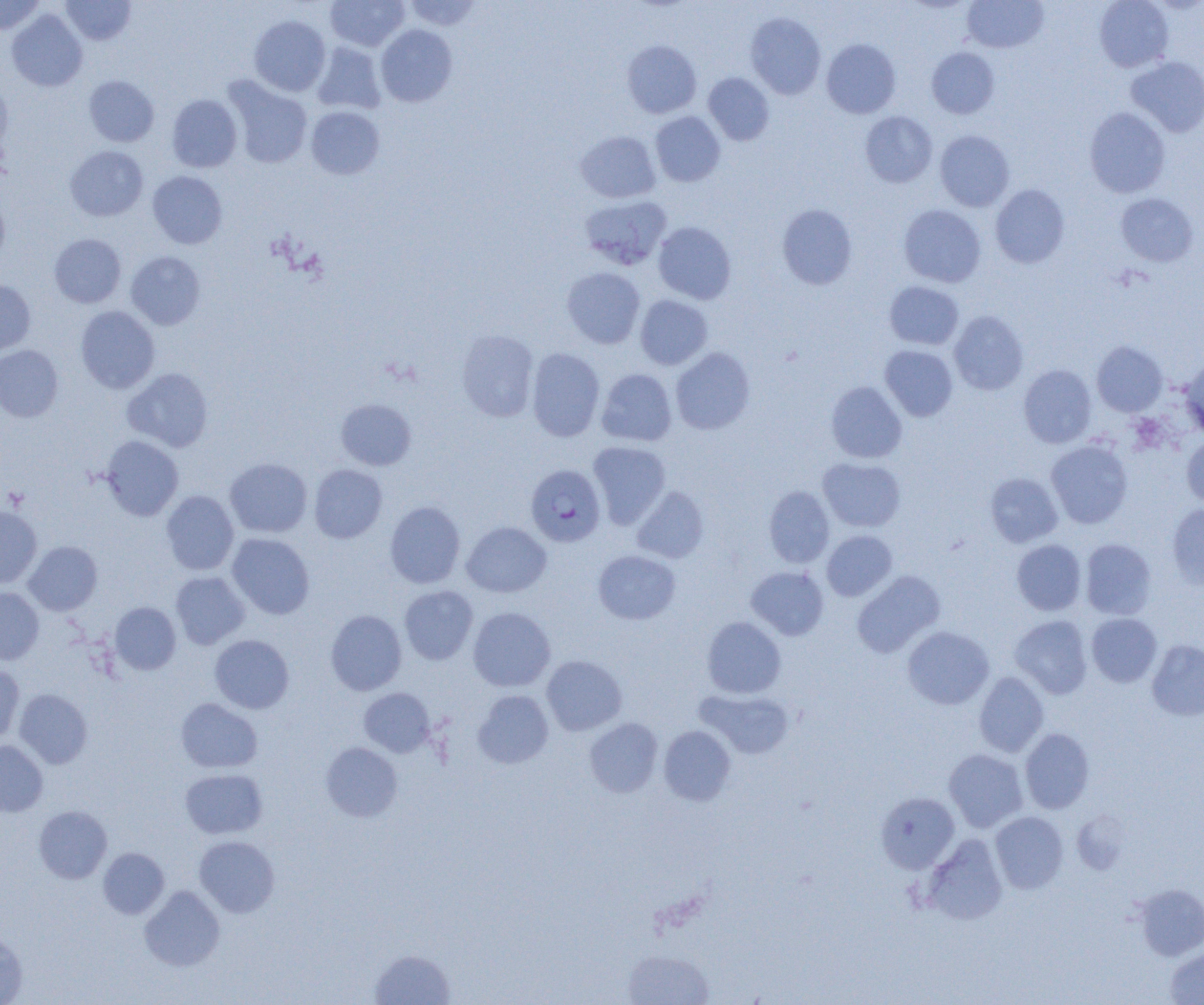
Summary:
  - Coordinate format: approximate bounding boxes as (x1,y1)-(x2,y2) corner pairs in pixels
  - Platelet locations: (3,486)-(30,511)
  - Uninfected red blood cell locations: (1,0)-(46,36), (60,0)-(137,46), (326,0)-(409,51), (404,0)-(483,31), (962,0)-(1048,53), (1094,0)-(1173,72), (6,9)-(88,92), (746,13)-(825,99), (249,15)-(331,96), (376,24)-(457,107), (822,39)-(901,118), (622,40)-(701,118), (312,41)-(386,114), (926,47)-(999,118), (1126,56)-(1204,137), (703,73)-(774,145), (83,75)-(159,147), (223,76)-(313,169), (0,78)-(13,160), (167,94)-(242,172), (306,106)-(384,179), (1084,107)-(1171,198), (650,111)-(725,187), (860,111)-(937,188), (575,130)-(660,203), (935,130)-(1014,212), (65,145)-(148,221), (147,171)-(227,249), (990,184)-(1070,268), (0,193)-(10,267), (1115,193)-(1198,267), (580,195)-(672,269), (777,204)-(857,289), (898,204)-(985,287), (653,222)-(736,304), (49,234)-(126,308), (126,251)-(206,330), (562,267)-(645,349), (0,279)-(36,355), (884,281)-(964,350), (635,295)-(712,370), (76,305)-(160,393), (949,310)-(1028,395), (456,329)-(539,421), (1092,341)-(1167,416), (0,345)-(63,422), (880,345)-(958,421), (671,347)-(755,434), (527,348)-(605,441), (1179,358)-(1204,435), (1018,364)-(1097,448), (123,367)-(213,452), (597,368)-(677,446), (826,381)-(907,463), (336,398)-(417,471), (1182,433)-(1204,509), (101,435)-(183,520), (1045,439)-(1133,528), (588,441)-(671,527), (818,457)-(906,531), (224,458)-(312,537), (309,464)-(387,543), (985,472)-(1063,547), (632,486)-(709,564), (763,486)-(834,568), (161,490)-(239,575), (385,501)-(465,588), (1167,503)-(1204,590), (0,506)-(42,589), (461,521)-(551,597), (821,530)-(897,601), (227,533)-(314,619), (1080,538)-(1157,620), (1011,539)-(1086,615), (24,541)-(102,615), (593,550)-(680,625), (746,566)-(829,640), (852,570)-(945,658), (170,571)-(250,649), (399,585)-(478,664), (0,587)-(44,664), (110,602)-(181,674), (468,606)-(556,691), (325,610)-(407,695), (1086,613)-(1162,687), (1010,615)-(1092,699), (701,616)-(786,698), (902,626)-(994,709), (210,634)-(294,714), (1147,639)-(1204,721), (541,655)-(627,736), (0,665)-(24,744), (974,672)-(1049,757), (359,687)-(435,757), (14,689)-(93,768), (696,689)-(794,759), (473,690)-(554,769), (176,698)-(263,772), (585,718)-(663,797), (658,725)-(736,805), (1020,728)-(1094,813), (0,740)-(48,817), (321,742)-(402,822), (943,748)-(1028,832), (180,769)-(267,839), (876,792)-(959,873), (34,805)-(112,883), (990,811)-(1068,894), (922,834)-(1008,925), (194,835)-(280,917), (99,847)-(169,919), (1134,883)-(1204,960), (140,885)-(224,971), (0,930)-(27,1004), (1165,947)-(1204,1004), (369,949)-(456,1005), (623,949)-(714,1005)
  - Plasmodium falciparum-infected red blood cell locations: (525,464)-(606,547)
  - Slide-level diagnosis: Plasmodium falciparum
  - Modality: light microscopy
  - Image size: 1204×1005 pixels
  - Preparation: thin blood film
  - Field of view: single
  - Magnification: 1000x